Give the preparation type.
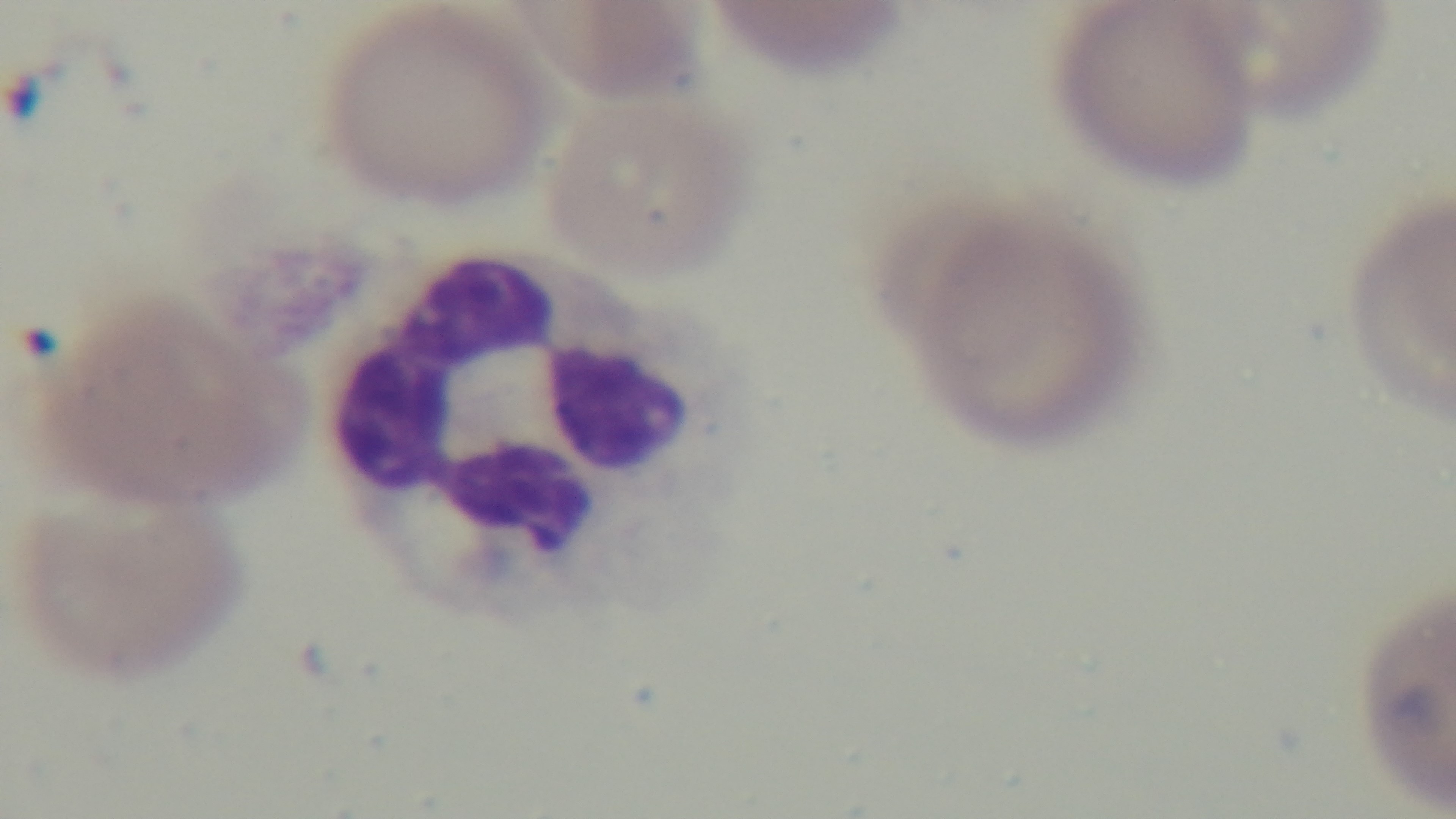
Thin.

Single field of view. Photomicrograph. Giemsa-stained. Malaria status: infected. Captured with a mounted 4K digital camera. 100x oil-immersion objective.